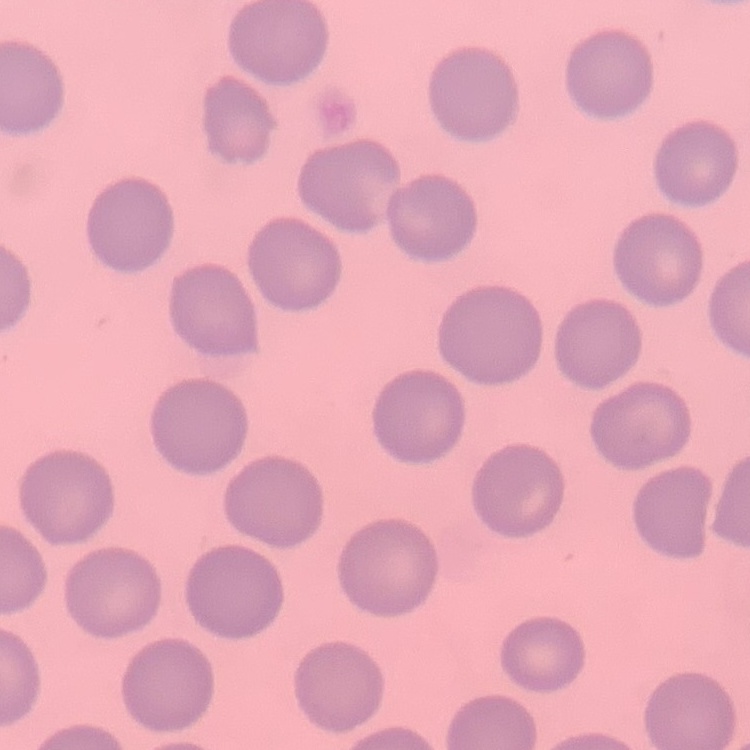

The erythrocytes exhibit no rouleaux formation. Stained with either Field's or Giemsa. Thin peripheral smear. Square crop of a larger photomicrograph.